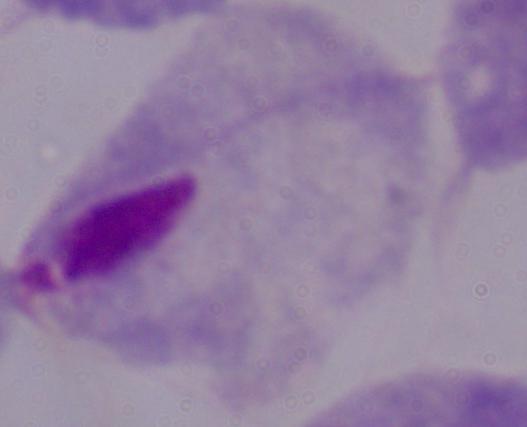

Summary:
  - Identification: trichomonad
  - Modality: photomicrograph
  - Magnification: 1000x